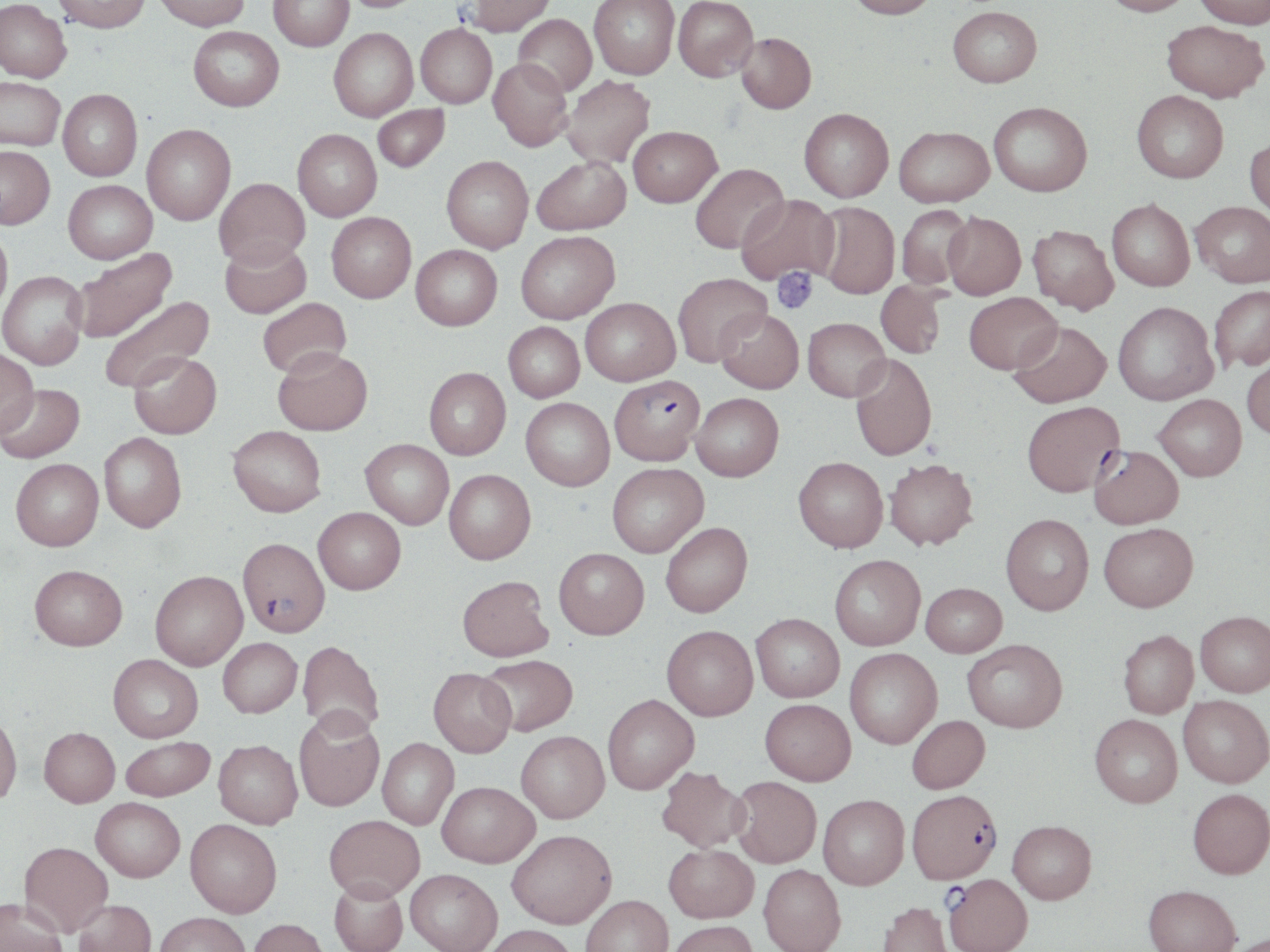

Summary:
  - Coordinate format: approximate bounding boxes as (x1, y1, x2, y2) in pixels
  - Platelet locations: (772, 267, 818, 314)
  - Plasmodium falciparum-infected red blood cell locations: (609, 374, 704, 465), (1089, 445, 1184, 529), (238, 537, 330, 636), (907, 789, 1002, 883), (944, 873, 1032, 952)
  - Uninfected red blood cell locations: (0, 0, 71, 84), (51, 0, 151, 34), (154, 0, 250, 32), (268, 0, 354, 51), (339, 0, 428, 14), (464, 0, 556, 38), (589, 0, 679, 80), (673, 0, 758, 82), (846, 0, 938, 22), (1100, 0, 1194, 20), (1194, 0, 1270, 32), (948, 9, 1042, 92), (513, 15, 597, 97), (1161, 23, 1268, 107), (416, 24, 497, 108), (188, 27, 283, 113), (329, 28, 418, 122), (736, 33, 816, 115), (487, 58, 572, 151), (561, 76, 656, 168), (0, 78, 65, 151), (58, 89, 142, 181), (1132, 94, 1228, 186), (372, 104, 449, 172), (988, 105, 1092, 200), (799, 109, 893, 203), (142, 124, 235, 224), (628, 126, 722, 207), (292, 129, 382, 221), (894, 129, 994, 210), (1244, 141, 1270, 226), (0, 146, 55, 229), (442, 155, 533, 253), (532, 156, 630, 234), (690, 163, 788, 254), (214, 178, 310, 268), (63, 180, 157, 263), (736, 194, 839, 286), (1107, 201, 1195, 293), (814, 203, 899, 300), (1191, 203, 1270, 290), (897, 205, 973, 291), (326, 212, 416, 303), (943, 214, 1025, 302), (1027, 226, 1118, 316), (0, 227, 12, 319), (516, 230, 620, 323), (219, 239, 311, 319), (411, 244, 502, 330), (69, 249, 176, 343), (0, 270, 88, 370), (672, 273, 770, 367), (876, 281, 946, 359), (1210, 287, 1270, 373), (964, 294, 1061, 376), (98, 295, 215, 393), (257, 297, 351, 378), (580, 297, 680, 385), (1113, 303, 1218, 406), (715, 308, 803, 393), (803, 318, 890, 401), (503, 322, 584, 402), (1008, 322, 1111, 408), (273, 347, 372, 435), (0, 349, 38, 437), (129, 351, 222, 438), (850, 355, 937, 461), (1242, 357, 1270, 441), (424, 367, 510, 459), (0, 383, 85, 464), (692, 393, 783, 481), (1153, 394, 1247, 480), (521, 398, 614, 490), (1022, 401, 1124, 497), (228, 425, 326, 516), (99, 432, 187, 532), (361, 439, 453, 529), (793, 457, 888, 552), (10, 458, 103, 550), (884, 458, 978, 550), (607, 463, 708, 557), (444, 469, 536, 564), (313, 507, 406, 594), (1001, 514, 1094, 615), (661, 522, 752, 617), (1099, 522, 1198, 612), (554, 548, 649, 638), (829, 554, 926, 650), (29, 564, 127, 650), (150, 570, 248, 670), (458, 575, 553, 661), (921, 582, 1007, 656), (1196, 611, 1270, 697), (751, 613, 844, 702), (662, 625, 758, 720), (1118, 630, 1198, 718), (218, 637, 302, 717), (962, 638, 1067, 732), (297, 639, 384, 736), (845, 648, 942, 748), (108, 654, 203, 742), (480, 654, 578, 735), (429, 667, 516, 757), (603, 694, 699, 794), (1178, 695, 1270, 787), (760, 698, 856, 785), (293, 709, 384, 811), (0, 710, 22, 804), (1090, 714, 1182, 807), (907, 715, 989, 793), (39, 727, 120, 806), (516, 730, 609, 822), (120, 736, 215, 801), (377, 738, 458, 828), (214, 739, 302, 828), (656, 766, 749, 852), (730, 776, 822, 867), (437, 780, 539, 866), (1188, 788, 1270, 878), (818, 794, 909, 889), (91, 797, 185, 881), (324, 814, 424, 900), (185, 819, 282, 917), (1008, 820, 1096, 904), (507, 829, 617, 928), (19, 841, 113, 936), (664, 843, 758, 922), (759, 864, 846, 952), (405, 868, 502, 952), (329, 878, 408, 952), (1144, 884, 1240, 952), (581, 894, 674, 952), (0, 898, 67, 952), (74, 899, 156, 952), (878, 900, 954, 952), (154, 911, 250, 952), (248, 918, 328, 952), (667, 920, 758, 952), (481, 924, 579, 952), (1225, 933, 1270, 952)
  - Slide-level diagnosis: Plasmodium falciparum
  - Magnification: 1000x
  - Image size: 1270×952 pixels
  - Stain: May-Grünwald-Giemsa
  - Field of view: one of a larger specimen
  - Preparation: thin blood film
  - Modality: light microscopy